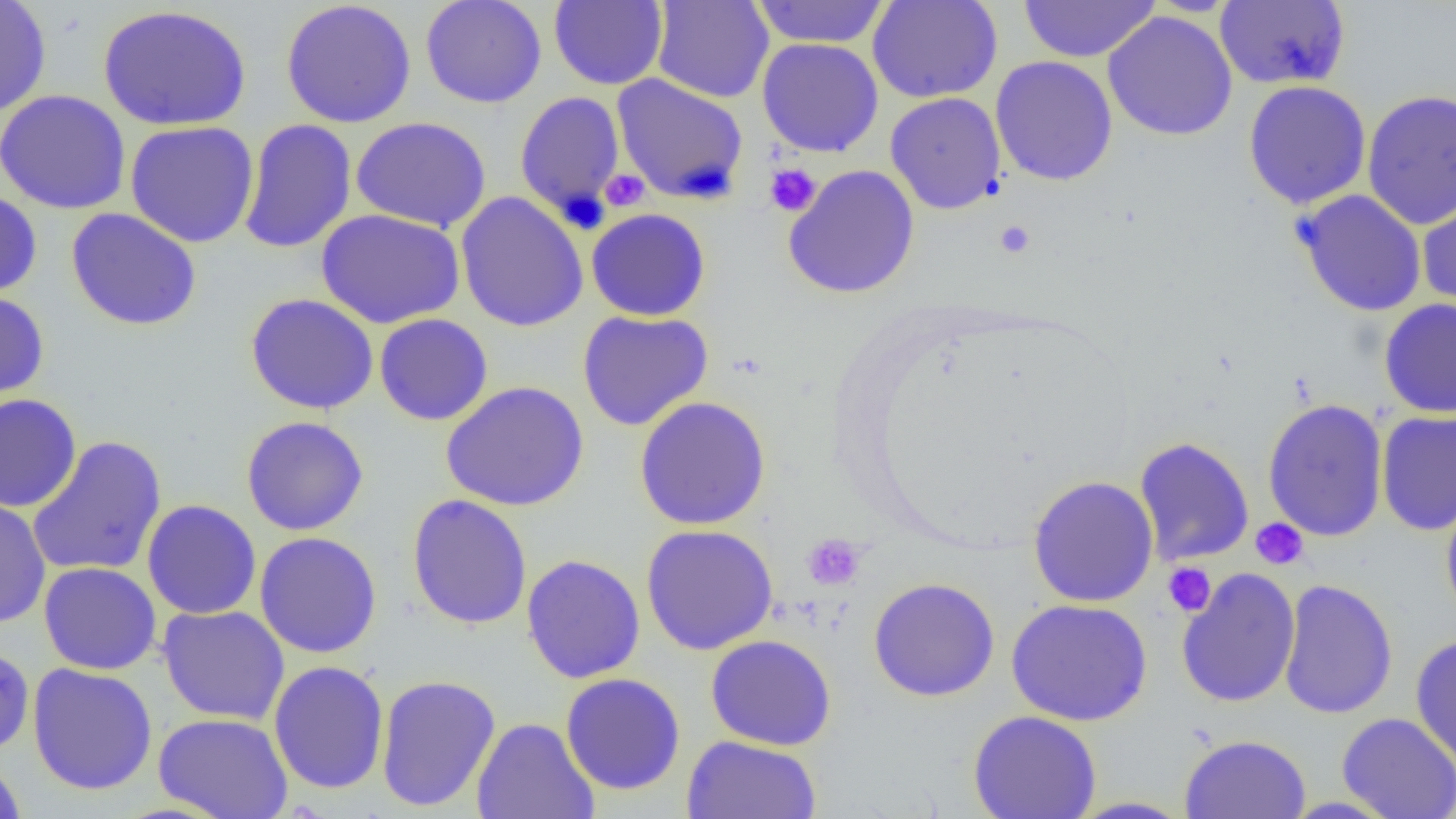
Summary:
  - Coordinate format: approximate bounding boxes as named x1/y1/x2/y2 corners in pixels
  - Platelet locations: (x1=763, y1=163, x2=821, y2=217), (x1=600, y1=169, x2=649, y2=211), (x1=994, y1=220, x2=1036, y2=259), (x1=1251, y1=517, x2=1309, y2=570), (x1=802, y1=534, x2=865, y2=590), (x1=1163, y1=562, x2=1216, y2=616)
  - Uninfected red blood cell locations: (x1=0, y1=0, x2=52, y2=117), (x1=280, y1=0, x2=417, y2=128), (x1=420, y1=0, x2=547, y2=108), (x1=550, y1=0, x2=668, y2=90), (x1=651, y1=0, x2=774, y2=103), (x1=750, y1=0, x2=891, y2=48), (x1=867, y1=0, x2=1003, y2=103), (x1=1017, y1=0, x2=1161, y2=63), (x1=1215, y1=1, x2=1350, y2=90), (x1=98, y1=4, x2=252, y2=131), (x1=1102, y1=11, x2=1238, y2=141), (x1=757, y1=38, x2=884, y2=158), (x1=990, y1=56, x2=1118, y2=186), (x1=612, y1=74, x2=749, y2=204), (x1=1243, y1=80, x2=1372, y2=209), (x1=1362, y1=89, x2=1456, y2=229), (x1=0, y1=90, x2=131, y2=214), (x1=514, y1=90, x2=626, y2=224), (x1=885, y1=92, x2=1006, y2=214), (x1=350, y1=116, x2=491, y2=232), (x1=238, y1=119, x2=358, y2=254), (x1=124, y1=120, x2=260, y2=248), (x1=783, y1=164, x2=920, y2=299), (x1=0, y1=189, x2=42, y2=299), (x1=1294, y1=189, x2=1428, y2=317), (x1=455, y1=191, x2=589, y2=332), (x1=1416, y1=191, x2=1456, y2=317), (x1=65, y1=208, x2=202, y2=331), (x1=586, y1=208, x2=711, y2=321), (x1=316, y1=209, x2=465, y2=329), (x1=0, y1=291, x2=50, y2=406), (x1=245, y1=293, x2=379, y2=415), (x1=1379, y1=298, x2=1456, y2=418), (x1=577, y1=310, x2=713, y2=431), (x1=374, y1=313, x2=494, y2=426), (x1=441, y1=380, x2=589, y2=511), (x1=0, y1=393, x2=82, y2=513), (x1=633, y1=396, x2=771, y2=530), (x1=1262, y1=398, x2=1389, y2=541), (x1=1376, y1=410, x2=1456, y2=536), (x1=241, y1=416, x2=369, y2=535), (x1=26, y1=435, x2=168, y2=578), (x1=1134, y1=436, x2=1254, y2=566), (x1=1028, y1=475, x2=1159, y2=607), (x1=1440, y1=489, x2=1456, y2=628), (x1=407, y1=494, x2=533, y2=630), (x1=0, y1=495, x2=51, y2=629), (x1=142, y1=499, x2=262, y2=619), (x1=641, y1=524, x2=779, y2=655), (x1=255, y1=531, x2=382, y2=658), (x1=521, y1=553, x2=646, y2=684), (x1=39, y1=562, x2=161, y2=675), (x1=1176, y1=567, x2=1301, y2=708), (x1=868, y1=577, x2=1000, y2=702), (x1=1278, y1=578, x2=1398, y2=720), (x1=1006, y1=598, x2=1153, y2=727), (x1=157, y1=605, x2=290, y2=725), (x1=705, y1=634, x2=836, y2=750), (x1=1410, y1=634, x2=1456, y2=769), (x1=0, y1=645, x2=35, y2=757), (x1=268, y1=660, x2=390, y2=794), (x1=27, y1=663, x2=158, y2=796), (x1=560, y1=673, x2=685, y2=795), (x1=375, y1=674, x2=501, y2=812), (x1=968, y1=710, x2=1102, y2=819), (x1=153, y1=712, x2=293, y2=819), (x1=1337, y1=712, x2=1456, y2=819), (x1=471, y1=717, x2=599, y2=819), (x1=1180, y1=734, x2=1311, y2=819), (x1=681, y1=735, x2=821, y2=819), (x1=0, y1=754, x2=27, y2=818), (x1=1066, y1=796, x2=1197, y2=818)
  - Slide-level diagnosis: no evidence of blood parasites
  - Field of view: one of a larger specimen
  - Image size: 1456×819 pixels
  - Modality: light microscopy
  - Preparation: thin blood film
  - Magnification: 1000x